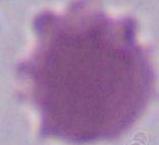
{
  "modality": "photomicrograph",
  "magnification": "1000x",
  "identification": "erythrocyte"
}